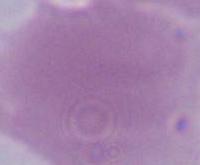

Captured at 1000x magnification. Photomicrograph. An erythrocyte is shown.